Assess the morphology of the erythrocytes.
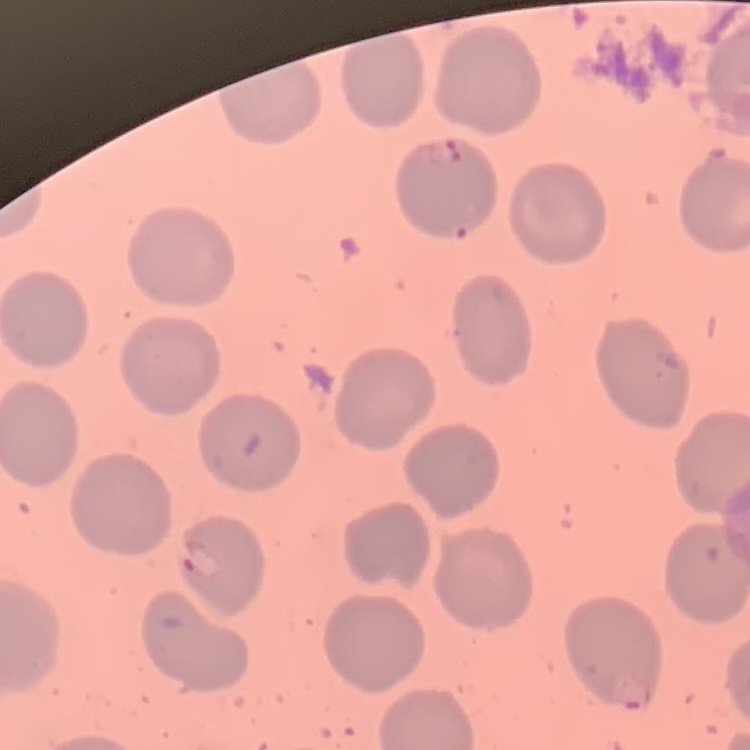

They show no rouleaux formation.

Field's or Giemsa stain. One tile cut from a larger photomicrograph. Thin blood film.